Point out each Plasmodium parasite.
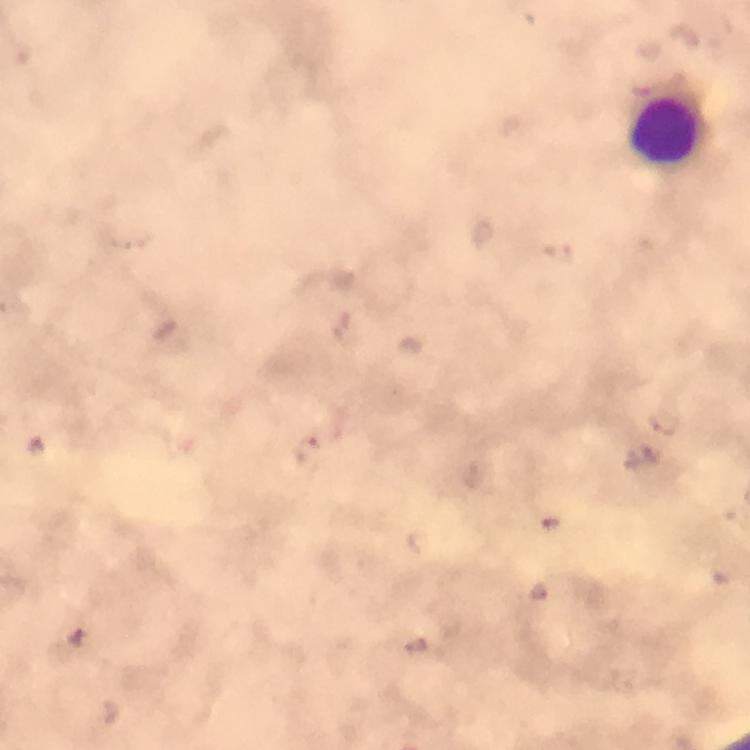

No Plasmodium parasites detected.

magnification = 100x
image size = 750×750 pixels
preparation = thick blood smear
capture = smartphone camera through the microscope
immersion oil = applied
context = from a malaria diagnostic workup
leukocyte locations = approximate centers as [x, y] in pixels: [664, 130]
cropped from = one field of view
stain = Giemsa